Identify the parasite.
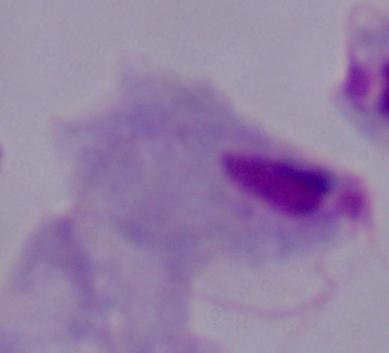
A trichomonad.

Captured at 1000x magnification. Photomicrograph.